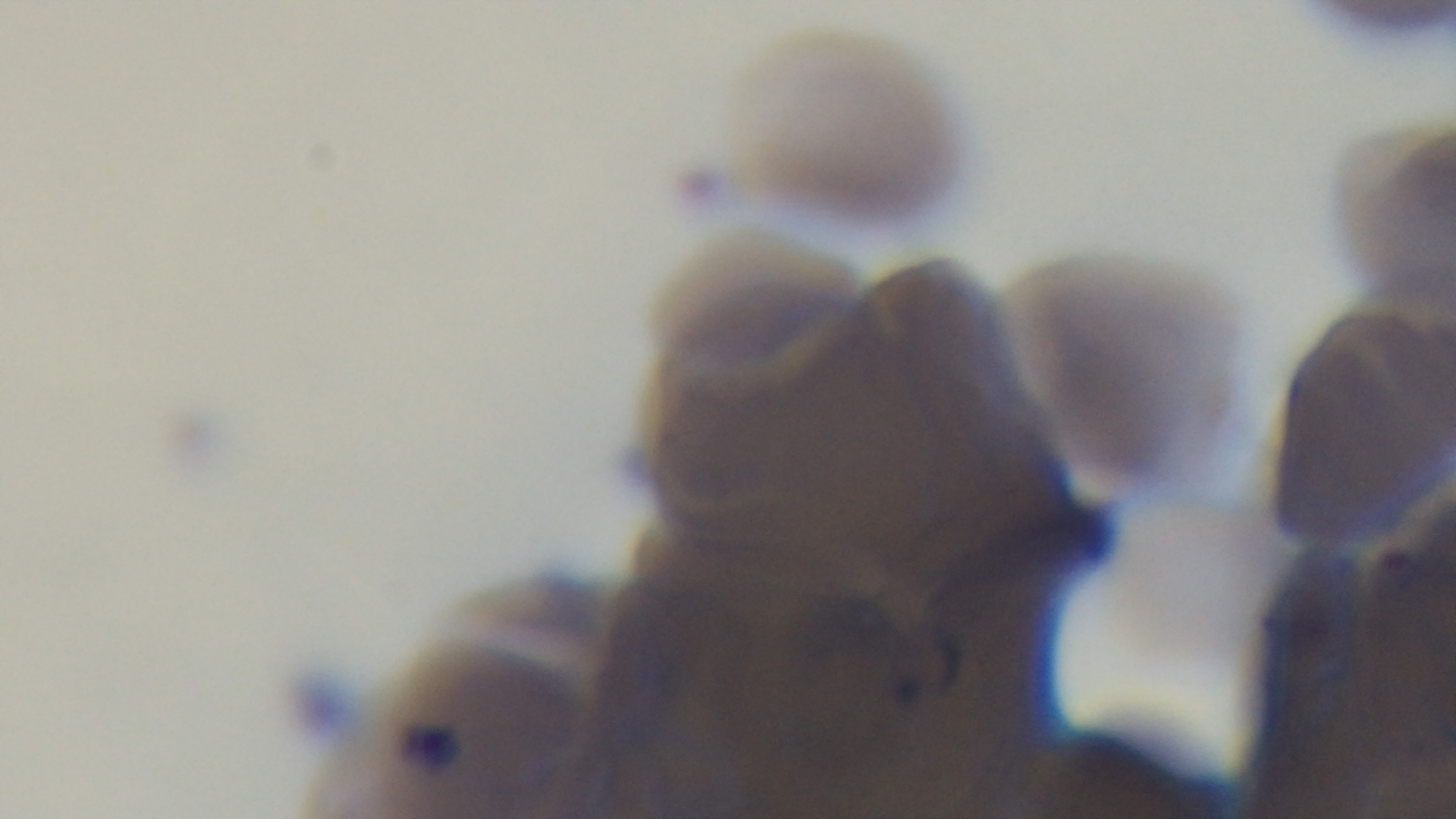
Summary:
  - Malaria status: infected
  - Capture: mounted 4K digital camera
  - Stain: Giemsa
  - Modality: light microscopy
  - Field of view: one from the slide
  - Preparation: thin blood film
  - Objective: 100x oil immersion